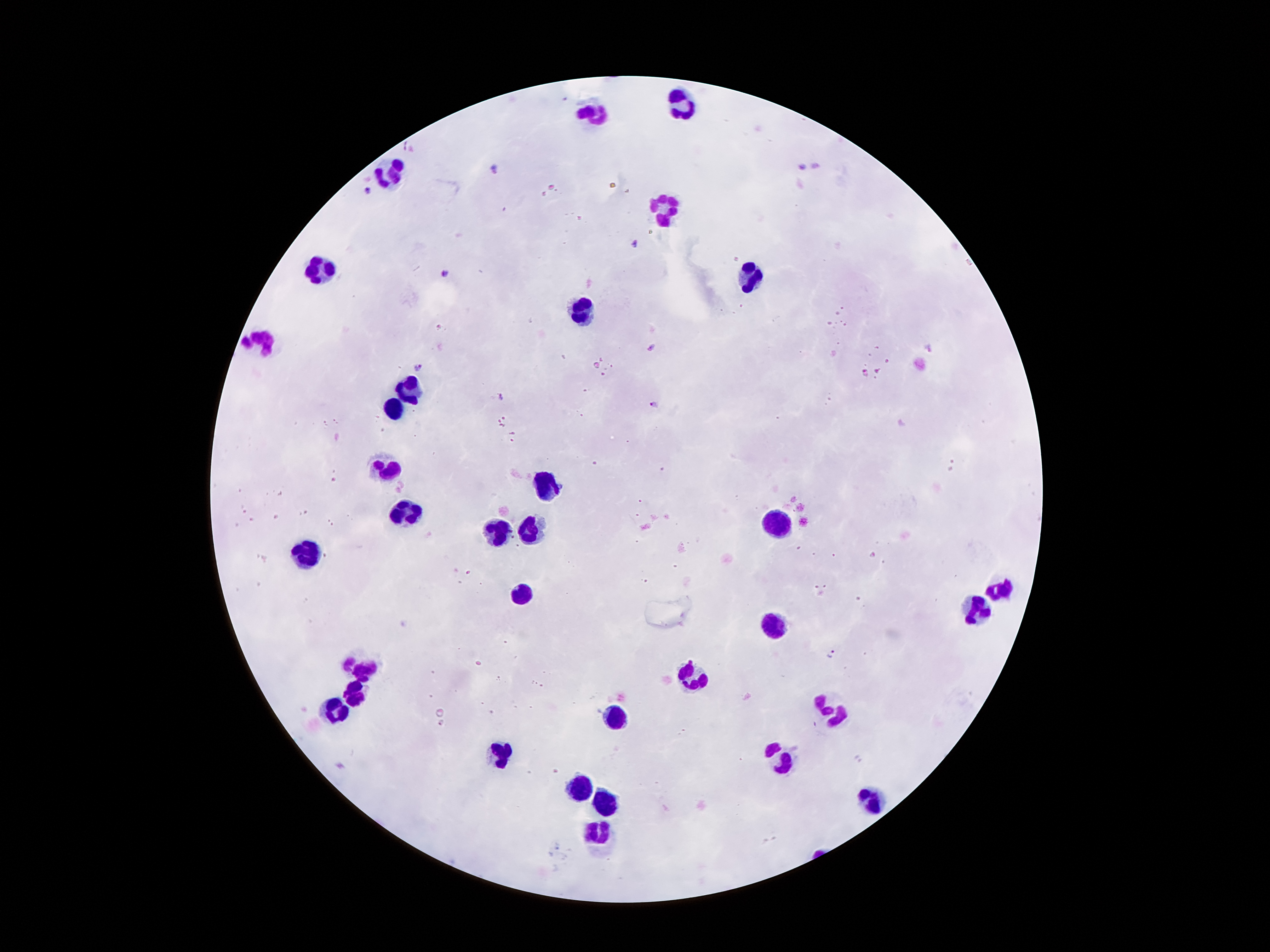
Approximate centers as (x, y) in pixels. Plasmodium parasite locations: (406, 144), (802, 167), (815, 168), (493, 169), (366, 189), (635, 243), (445, 273), (651, 346), (930, 350), (419, 366), (865, 373), (500, 396), (654, 403), (833, 654), (859, 758). Leukocyte locations: (682, 108), (589, 111), (393, 169), (661, 211), (321, 272), (752, 279), (584, 308), (264, 343), (409, 388), (394, 411), (387, 469), (545, 488), (405, 511), (779, 522), (499, 532), (534, 532), (310, 553), (526, 589), (995, 591), (972, 610), (776, 626), (363, 668), (696, 677), (355, 694), (829, 710), (337, 712), (618, 719), (502, 753), (776, 760), (582, 788), (608, 802), (869, 802), (597, 836). Patient malaria status: positive for Plasmodium falciparum. Thick peripheral-blood smear. Giemsa-stained preparation. Photographed through the microscope eyepiece with a smartphone camera. Image is 1270×952 pixels. 100x magnification. Single field of view.